Name the parasite shown.
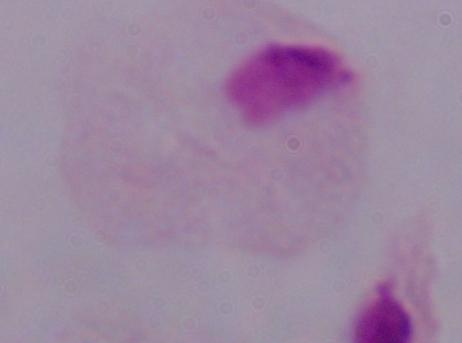
A trichomonad.

modality = photomicrograph
magnification = 1000x